Point out leukocytes.
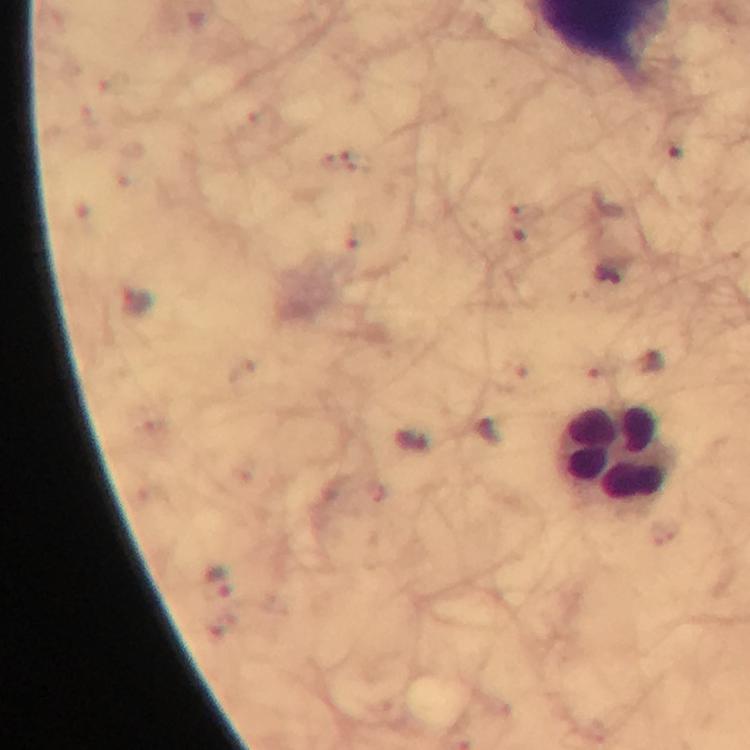
Approximate centers as {x, y} in pixels.
Leukocytes: {615, 454}.

capture = smartphone camera through the microscope
magnification = 100x
cropped from = one field of view
Plasmodium parasite locations = approximate centers as {x, y} in pixels: {607, 272}, {134, 301}, {489, 434}, {413, 440}, {217, 585}
image size = 750×750 pixels
context = from a malaria diagnostic workup
stain = Giemsa
preparation = thick blood film
immersion oil = applied